Point out each malaria parasite.
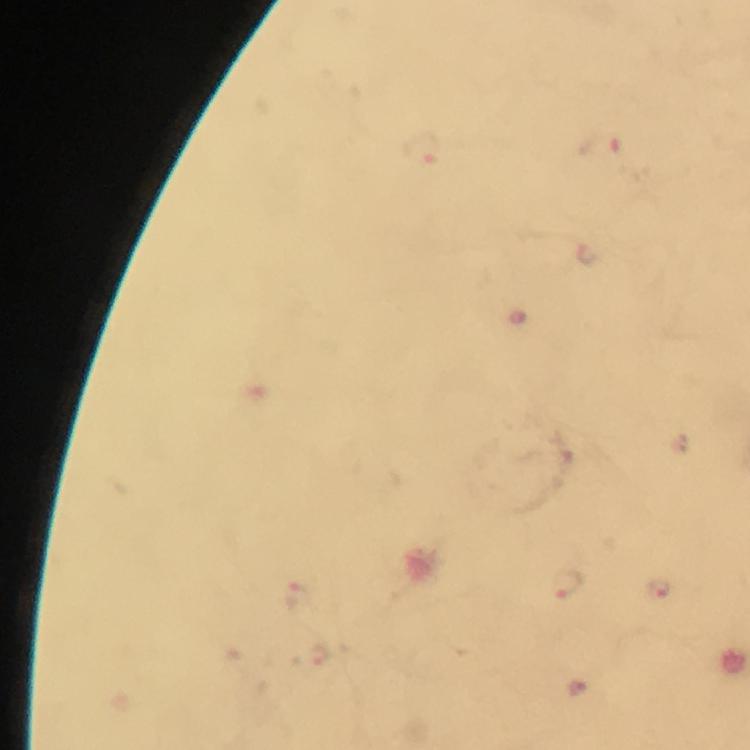

Approximate object centers, in pixels from the top-left corner.
Malaria parasites: (x=565, y=583), (x=657, y=590), (x=296, y=598), (x=318, y=658).

capture = smartphone photograph through a microscope
magnification = 100x
image size = 750×750 pixels
preparation = thick smear
immersion oil = applied
context = from a diagnostic examination for malaria
stain = Giemsa
cropped from = a single field of view